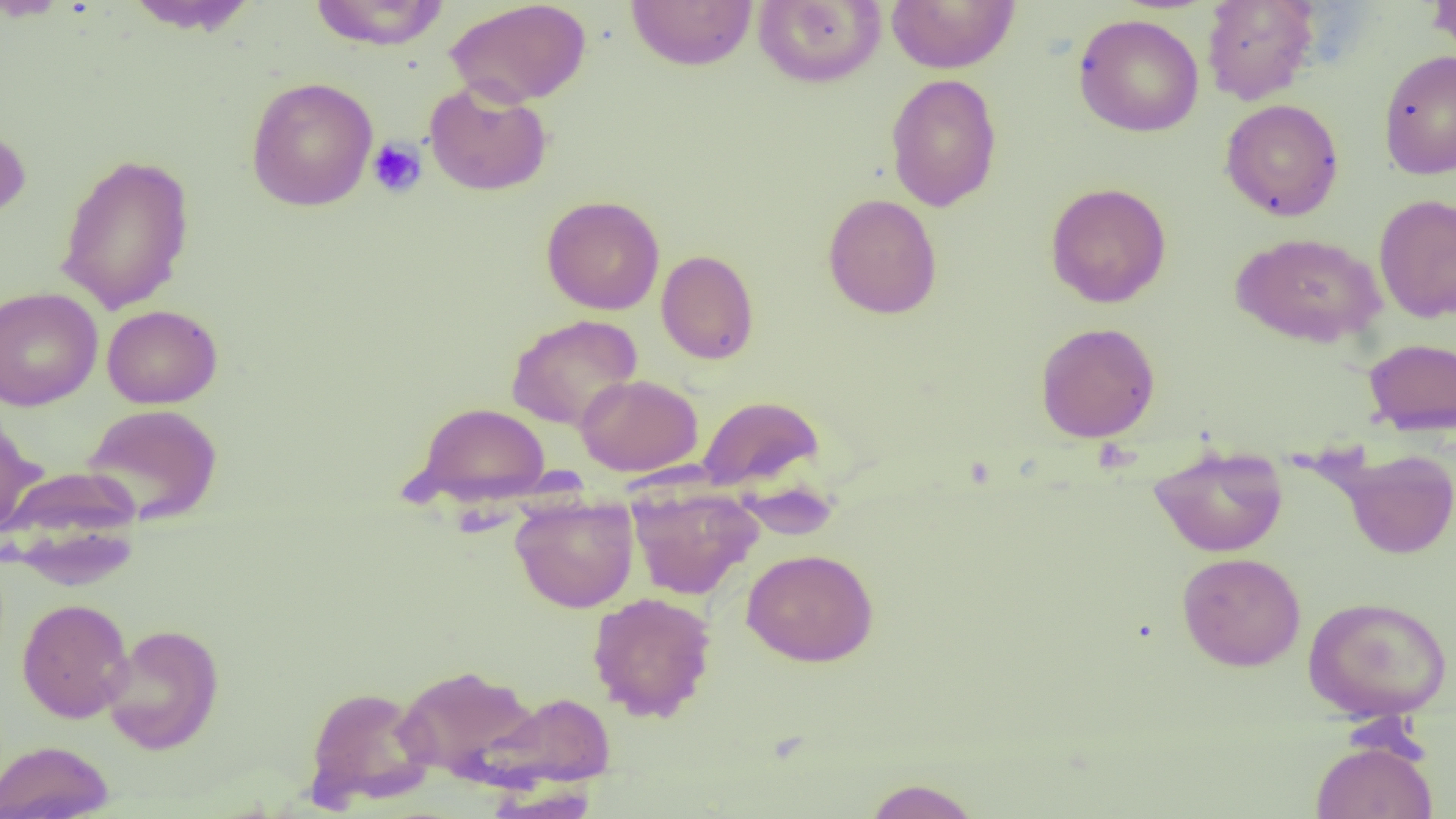 Approximate bounding boxes as named x1/y1/x2/y2 corners in pixels. Platelet locations: (x1=367, y1=138, x2=427, y2=198). Uninfected red blood cell locations: (x1=1, y1=0, x2=71, y2=21), (x1=123, y1=0, x2=261, y2=35), (x1=310, y1=0, x2=450, y2=51), (x1=445, y1=0, x2=592, y2=108), (x1=753, y1=0, x2=885, y2=88), (x1=886, y1=0, x2=1020, y2=73), (x1=1201, y1=0, x2=1320, y2=105), (x1=1428, y1=0, x2=1456, y2=59), (x1=626, y1=1, x2=757, y2=70), (x1=1073, y1=13, x2=1205, y2=137), (x1=1378, y1=49, x2=1456, y2=179), (x1=885, y1=74, x2=1002, y2=212), (x1=246, y1=77, x2=378, y2=211), (x1=424, y1=80, x2=552, y2=196), (x1=1220, y1=98, x2=1344, y2=221), (x1=0, y1=121, x2=31, y2=222), (x1=55, y1=152, x2=195, y2=314), (x1=1045, y1=182, x2=1172, y2=308), (x1=823, y1=193, x2=942, y2=319), (x1=1373, y1=194, x2=1456, y2=324), (x1=541, y1=195, x2=665, y2=315), (x1=1231, y1=231, x2=1385, y2=347), (x1=657, y1=249, x2=759, y2=365), (x1=0, y1=286, x2=103, y2=411), (x1=102, y1=305, x2=222, y2=409), (x1=506, y1=313, x2=643, y2=431), (x1=1035, y1=322, x2=1160, y2=443), (x1=1363, y1=337, x2=1456, y2=435), (x1=575, y1=374, x2=702, y2=476), (x1=698, y1=395, x2=823, y2=491), (x1=411, y1=401, x2=550, y2=506), (x1=81, y1=404, x2=223, y2=525), (x1=0, y1=413, x2=45, y2=537), (x1=1149, y1=444, x2=1288, y2=557), (x1=1337, y1=449, x2=1456, y2=559), (x1=1, y1=467, x2=143, y2=581), (x1=627, y1=484, x2=762, y2=600), (x1=510, y1=495, x2=639, y2=613), (x1=742, y1=548, x2=879, y2=666), (x1=1176, y1=552, x2=1306, y2=671), (x1=587, y1=591, x2=717, y2=722), (x1=1303, y1=595, x2=1452, y2=721), (x1=17, y1=598, x2=133, y2=723), (x1=102, y1=624, x2=224, y2=755), (x1=395, y1=663, x2=543, y2=785), (x1=304, y1=685, x2=437, y2=808), (x1=481, y1=691, x2=615, y2=789), (x1=0, y1=740, x2=115, y2=819), (x1=1311, y1=740, x2=1437, y2=818), (x1=862, y1=777, x2=983, y2=818), (x1=485, y1=782, x2=601, y2=818). Slide-level diagnosis: no evidence of blood parasites. Captured at 1000x magnification. One field of a larger specimen. Image is 1456×819 pixels. Thin blood smear. Optical microscopy.